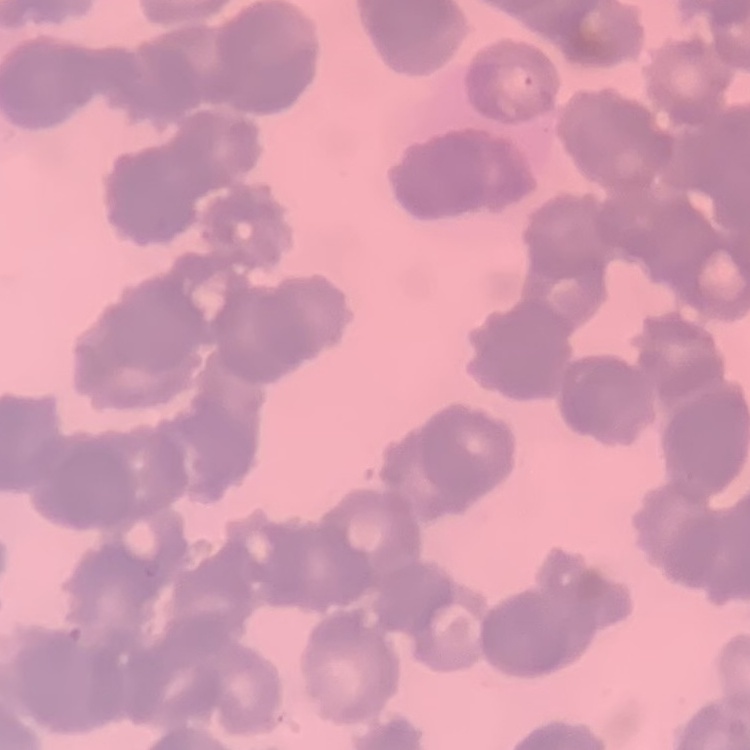

{
  "red_blood_cell_morphology": "rouleaux formation",
  "preparation": "thin peripheral smear",
  "stain": "Field's or Giemsa",
  "image_type": "one tile cut from a larger photomicrograph"
}